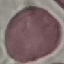

{
  "malaria_status": "uninfected",
  "preparation": "thin blood film",
  "capture": "smartphone through the microscope eyepiece",
  "stain": "Giemsa",
  "image_type": "cell patch, automatically extracted from a larger field of view and resized to 64 × 64 pixels"
}